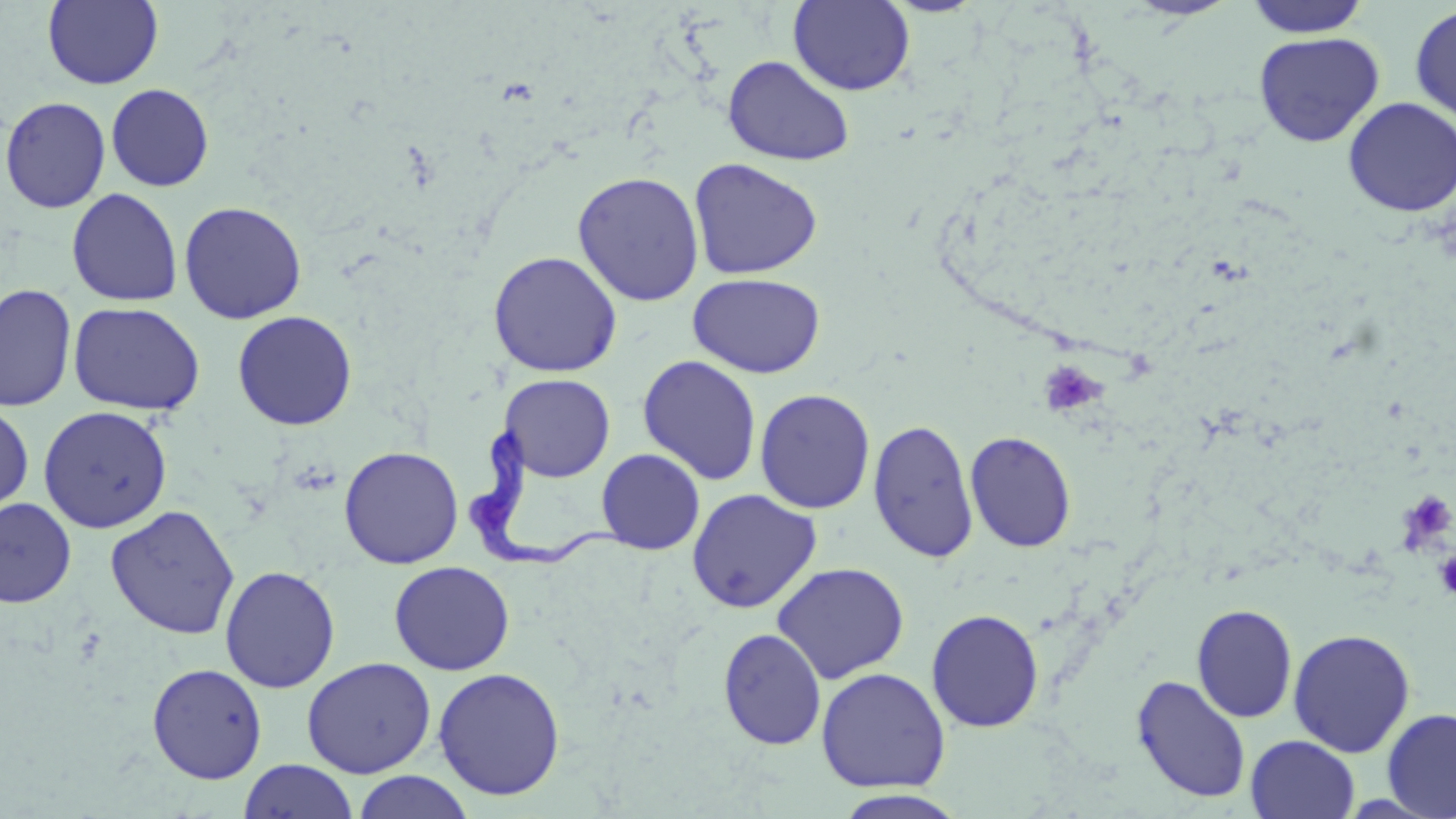

Summary:
  - Coordinate format: approximate bounding boxes as (x1,y1)-(x2,y2) corner pairs in pixels
  - Uninfected red blood cell locations: (42,0)-(164,89), (1123,0)-(1239,21), (1243,0)-(1372,38), (788,1)-(915,95), (1410,4)-(1456,126), (1253,31)-(1384,147), (722,54)-(855,167), (106,83)-(214,191), (0,95)-(111,213), (1343,96)-(1456,217), (688,157)-(823,280), (572,170)-(705,307), (66,188)-(183,307), (178,201)-(307,324), (487,250)-(623,377), (687,272)-(826,378), (0,283)-(77,412), (68,302)-(206,415), (232,310)-(357,430), (637,355)-(762,485), (498,373)-(615,482), (755,388)-(876,514), (0,402)-(34,517), (38,405)-(173,533), (867,419)-(979,563), (965,430)-(1077,552), (339,445)-(464,569), (596,448)-(706,554), (686,488)-(822,613), (0,497)-(77,608), (105,504)-(240,640), (388,561)-(516,675), (771,561)-(909,684), (219,565)-(340,693), (1191,603)-(1298,723), (926,608)-(1045,732), (718,627)-(826,750), (1287,627)-(1416,758), (301,656)-(436,778), (146,662)-(268,784), (815,666)-(950,793), (432,667)-(565,801), (1131,674)-(1251,803), (1381,708)-(1456,819), (1246,735)-(1360,818), (239,760)-(358,819), (352,771)-(474,819), (833,789)-(970,818)
  - Trypanosoma brucei locations: (464,417)-(635,575)
  - Platelet locations: (1037,361)-(1106,416), (1396,488)-(1456,552), (1434,550)-(1456,600)
  - Slide-level diagnosis: Trypanosoma brucei
  - Preparation: thin blood smear
  - Modality: optical microscopy
  - Magnification: 1000x
  - Image size: 1456×819 pixels
  - Field of view: one of a larger specimen
  - Stain: May-Grünwald-Giemsa